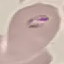

Summary:
  - Malaria status: parasitized
  - Capture: smartphone camera at the microscope eyepiece
  - Stain: Giemsa
  - Preparation: thin blood film
  - Image type: automatically extracted cell patch, resized to 64 × 64 pixels